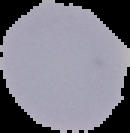
{
  "image_size": "130×133 pixels",
  "preparation": "thin blood film",
  "image_type": "segmented cell region with the area outside set to black",
  "malaria_status": "uninfected"
}